Identify the parasite.
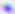

Toxoplasma gondii.

Captured at 400x magnification. Photomicrograph.